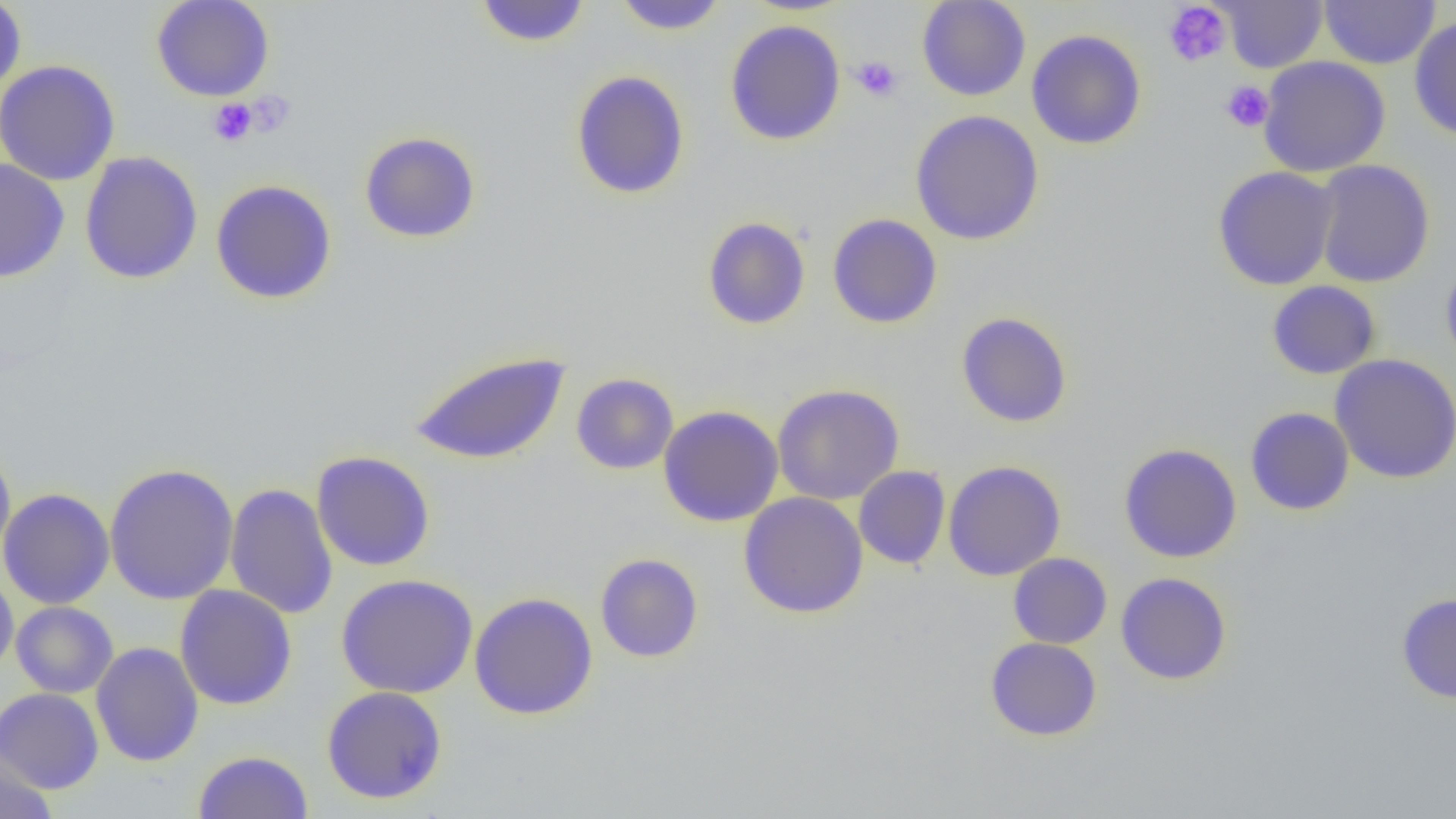

Summary:
  - Coordinate format: approximate bounding boxes as (x1, y1, x2, y2) in pixels
  - Platelet locations: (1163, 2, 1231, 67), (850, 55, 902, 102), (1220, 81, 1274, 132), (244, 91, 296, 136), (208, 99, 257, 147)
  - Uninfected red blood cell locations: (0, 0, 27, 97), (151, 0, 275, 101), (916, 0, 1031, 101), (1216, 0, 1328, 72), (1319, 0, 1441, 69), (473, 1, 592, 48), (612, 1, 729, 35), (1409, 16, 1456, 141), (724, 19, 845, 146), (1026, 29, 1146, 150), (1257, 56, 1390, 177), (0, 59, 120, 186), (570, 69, 690, 200), (910, 110, 1045, 245), (358, 130, 481, 244), (79, 151, 203, 285), (0, 158, 70, 283), (1312, 159, 1435, 288), (1212, 166, 1339, 290), (210, 179, 338, 305), (827, 213, 943, 329), (702, 216, 811, 330), (1440, 253, 1456, 373), (1266, 280, 1381, 380), (957, 312, 1073, 428), (408, 350, 572, 466), (1330, 354, 1456, 484), (571, 372, 679, 474), (772, 384, 904, 505), (657, 405, 783, 526), (1245, 407, 1355, 515), (1118, 443, 1242, 563), (0, 444, 16, 570), (311, 450, 435, 572), (942, 461, 1066, 581), (104, 462, 239, 605), (854, 466, 950, 569), (225, 482, 338, 620), (0, 487, 115, 609), (738, 492, 868, 618), (595, 553, 704, 662), (1008, 553, 1112, 649), (0, 570, 19, 679), (1116, 572, 1232, 685), (336, 574, 478, 698), (174, 584, 297, 710), (469, 592, 598, 720), (1396, 593, 1456, 704), (11, 601, 118, 698), (985, 637, 1102, 741), (90, 641, 203, 767), (321, 685, 448, 805), (0, 687, 104, 793), (194, 750, 313, 818), (0, 753, 57, 819)
  - Slide-level diagnosis: negative for blood parasites
  - Image size: 1456×819 pixels
  - Magnification: 1000x
  - Preparation: thin blood smear
  - Modality: optical microscopy
  - Field of view: single